Assess this cell for malaria.
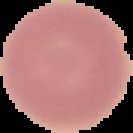

Uninfected.

preparation = thin blood film
image size = 133×133 pixels
image type = segmented cell region on a black background